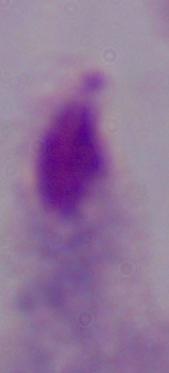

Captured at 1000x magnification. A trichomonad is shown. Photomicrograph.